State which parasite is depicted.
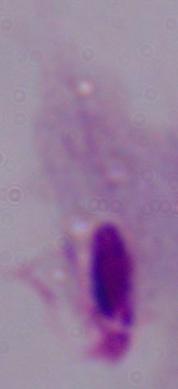

A trichomonad.

magnification: 1000x
modality: photomicrograph